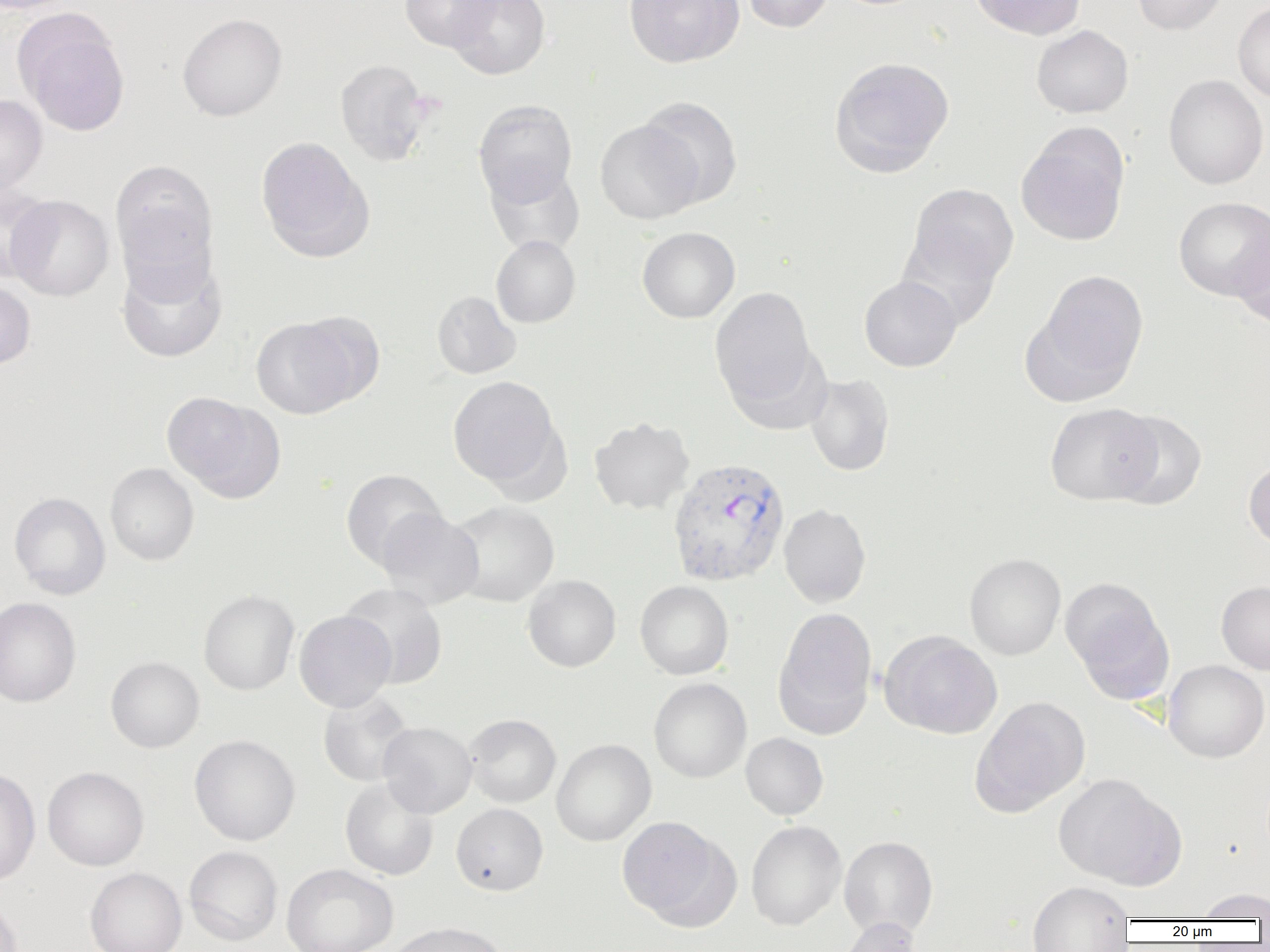
Summary:
  - Coordinate format: approximate bounding boxes as (x1, y1, x2, y2) in pixels
  - Uninfected red blood cell locations: (0, 0, 79, 14), (399, 0, 500, 51), (447, 0, 550, 79), (624, 0, 743, 68), (741, 0, 835, 33), (970, 0, 1086, 40), (1132, 0, 1229, 35), (1233, 2, 1270, 103), (177, 13, 287, 121), (15, 16, 131, 137), (1031, 25, 1134, 118), (829, 56, 955, 177), (335, 59, 431, 166), (1164, 75, 1268, 190), (0, 94, 47, 196), (639, 96, 742, 208), (473, 99, 577, 205), (595, 120, 702, 224), (1016, 128, 1129, 247), (256, 137, 373, 262), (110, 160, 218, 269), (484, 162, 585, 257), (0, 181, 54, 283), (906, 183, 1018, 289), (6, 194, 115, 301), (1174, 197, 1269, 300), (637, 227, 740, 323), (897, 227, 1006, 330), (1233, 227, 1270, 330), (491, 235, 581, 328), (115, 252, 228, 363), (1031, 269, 1149, 397), (859, 275, 961, 372), (0, 279, 36, 370), (709, 287, 819, 409), (431, 290, 521, 379), (295, 310, 385, 406), (251, 317, 358, 419), (804, 373, 895, 476), (447, 376, 563, 490), (161, 392, 284, 501), (1044, 402, 1160, 505), (1107, 410, 1208, 511), (589, 417, 695, 515), (1243, 458, 1270, 549), (105, 463, 199, 566), (340, 469, 447, 570), (9, 492, 110, 599), (446, 501, 560, 607), (779, 503, 871, 608), (376, 508, 484, 609), (964, 553, 1066, 660), (522, 574, 621, 672), (1062, 579, 1173, 700), (635, 580, 734, 680), (1216, 581, 1270, 674), (338, 583, 448, 689), (198, 589, 299, 695), (0, 597, 81, 707), (773, 607, 877, 738), (294, 610, 396, 712), (881, 632, 1003, 739), (105, 656, 205, 753), (1163, 660, 1269, 763), (648, 677, 751, 783), (317, 691, 415, 788), (970, 696, 1091, 816), (463, 714, 561, 808), (377, 722, 477, 818), (740, 733, 829, 820), (189, 734, 300, 846), (552, 739, 656, 846), (42, 766, 149, 871), (0, 767, 40, 886), (1053, 773, 1185, 889), (340, 777, 439, 881), (451, 803, 548, 895), (615, 815, 733, 926), (746, 820, 846, 930), (838, 835, 938, 939), (184, 845, 283, 945), (281, 863, 398, 952), (84, 867, 187, 952), (1027, 881, 1134, 951), (1194, 888, 1270, 920), (0, 895, 24, 952), (837, 917, 924, 952), (384, 921, 510, 952)
  - Plasmodium vivax-infected red blood cell locations: (667, 457, 790, 586)
  - Slide-level diagnosis: Plasmodium vivax
  - Modality: light microscopy
  - Preparation: thin blood smear
  - Image size: 1270×952 pixels
  - Magnification: 1000x
  - Field of view: one of a larger specimen